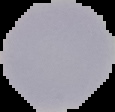
From a thin blood smear. Segmented cell region on a black background. Malaria status: uninfected. Image is 115×112 pixels.